Report the malaria status of this cell.
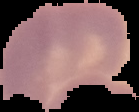
Uninfected.

Image is 139×112 pixels. Cell region segmented out of the field of view; the surrounding area is masked to black. From a thin blood smear.